Comment on the morphology of the erythrocytes.
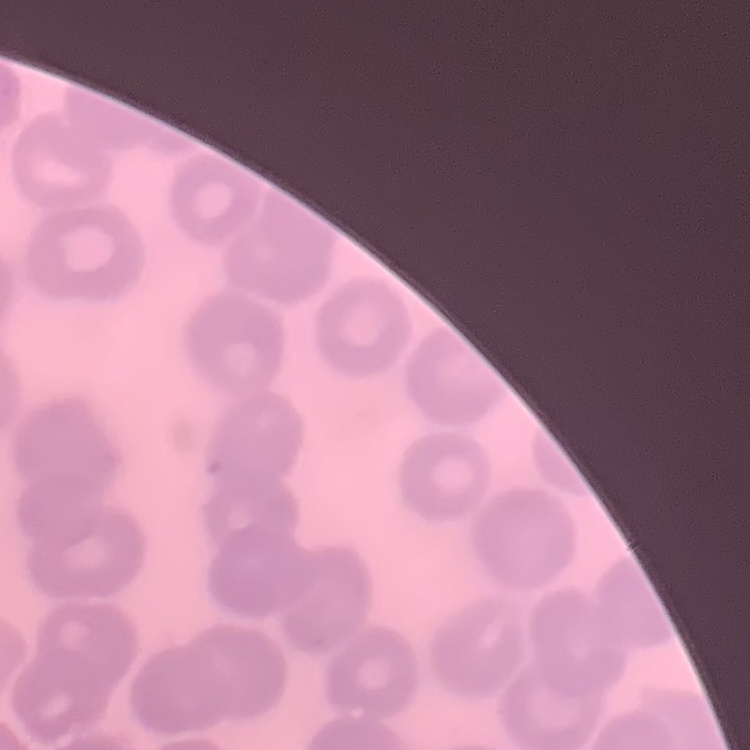

No rouleaux formation.

Summary:
  - Image type: square crop of a larger photomicrograph
  - Preparation: thin blood smear
  - Stain: Field's or Giemsa